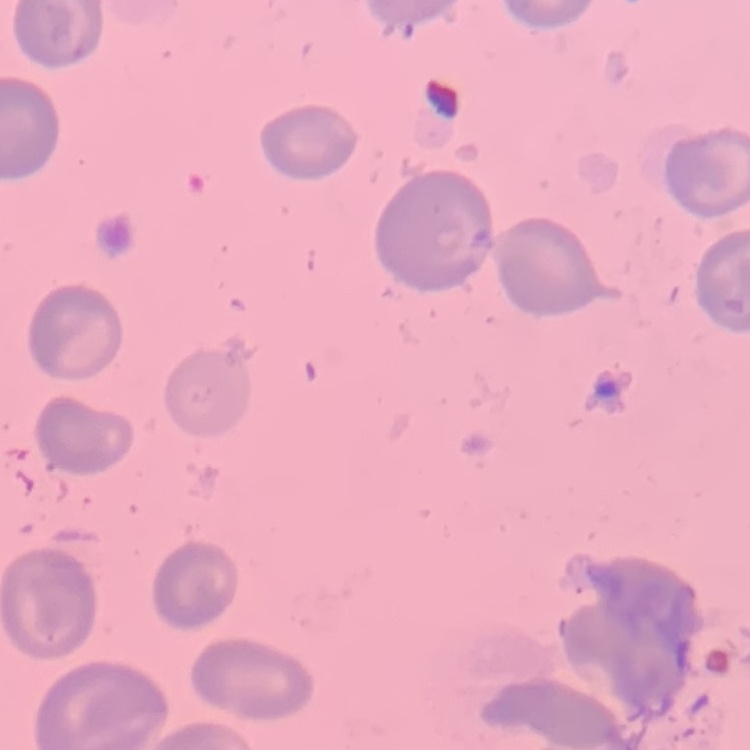
Summary:
  - Erythrocyte morphology: no rouleaux formation
  - Image type: square crop of a larger photomicrograph
  - Stain: Field's or Giemsa
  - Preparation: thin peripheral smear